Evaluate for Plasmodium parasites.
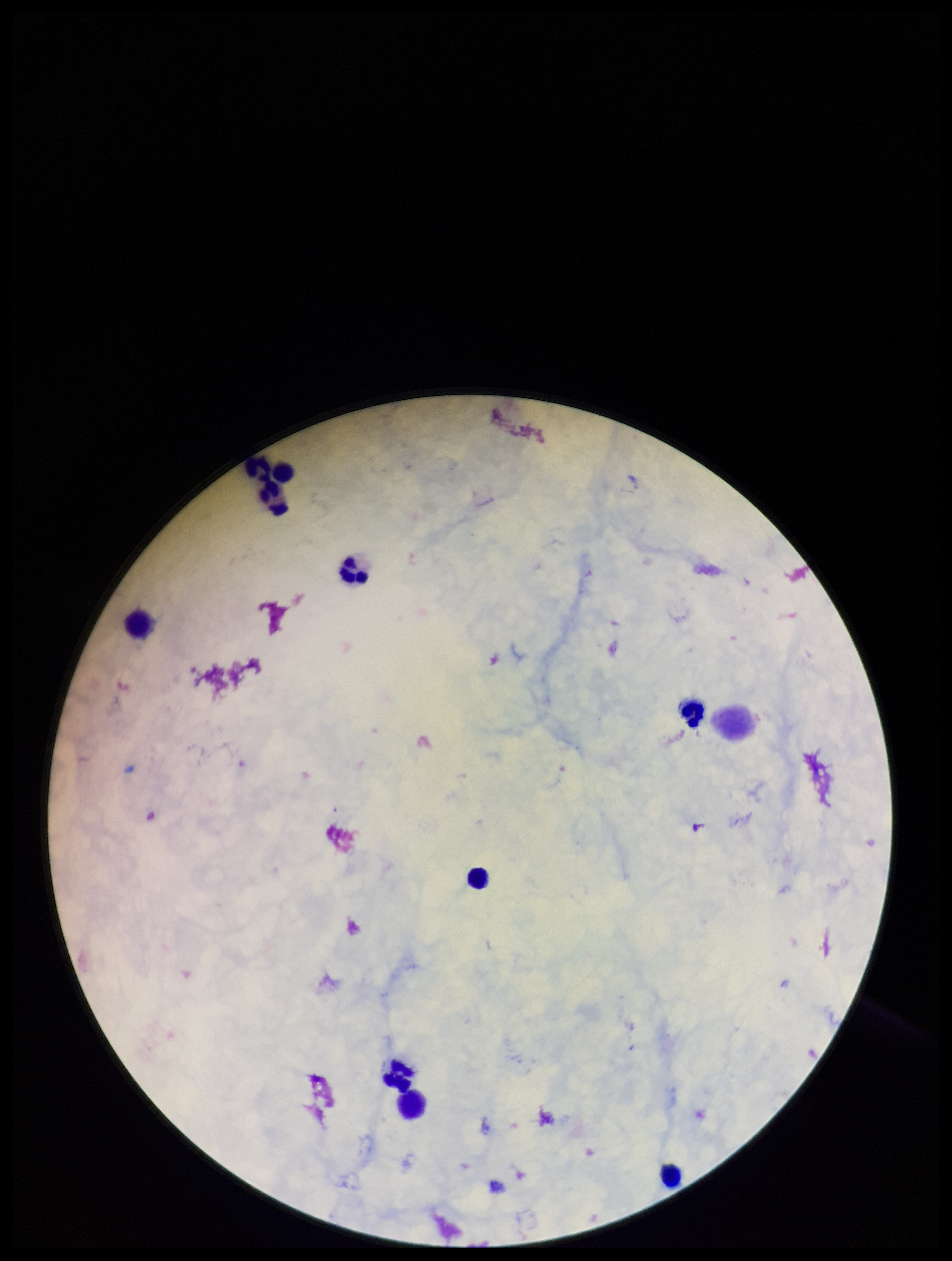

None identified.

Summary:
  - Field of view: one from this slide
  - Patient malaria status: negative
  - Capture: smartphone photograph through the microscope eyepiece
  - Leukocyte count: 10
  - Image size: 952×1261 pixels
  - Parasite count: 0
  - Stain: Giemsa
  - Preparation: thick